State the blood parasite species.
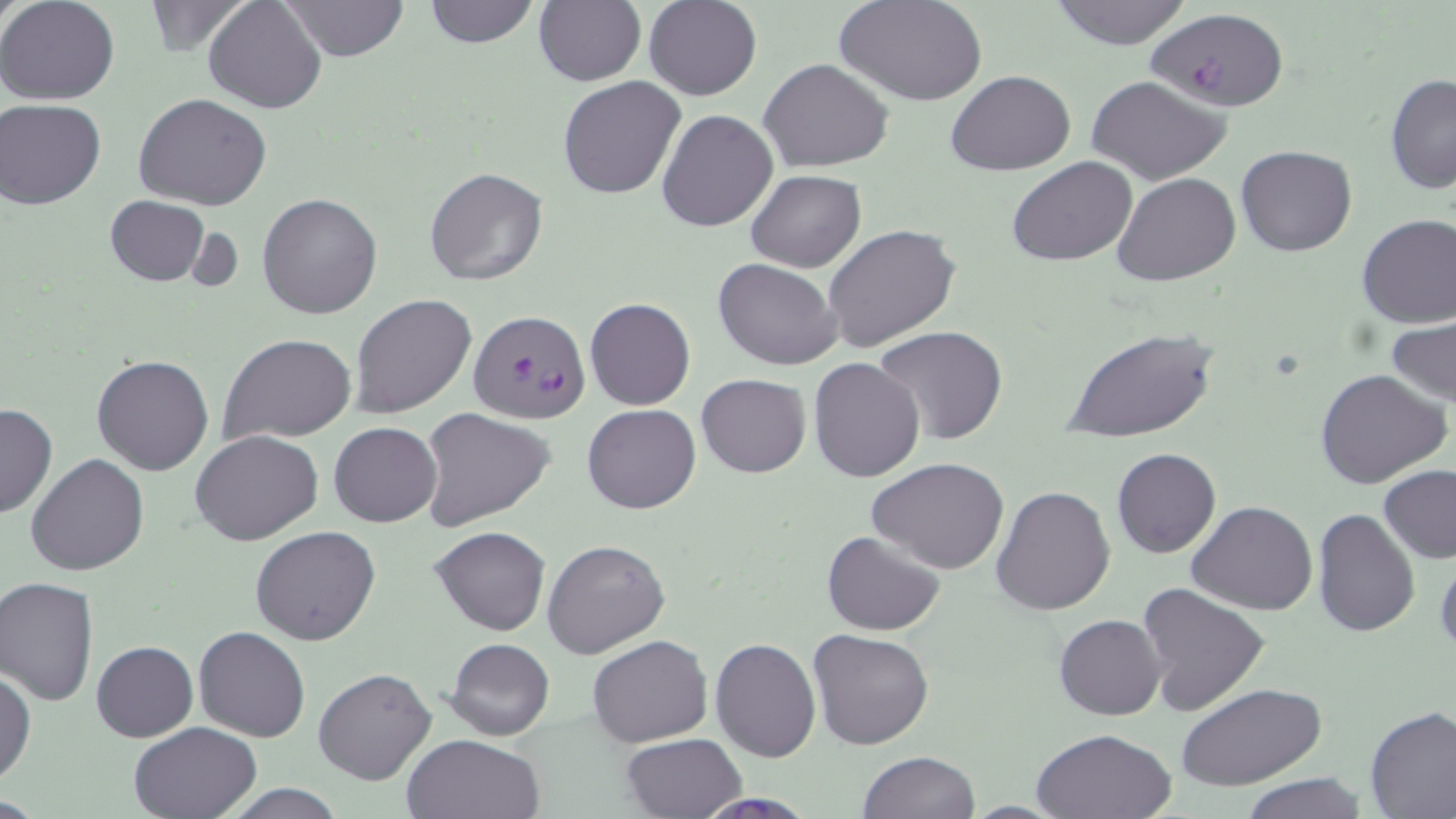
Plasmodium falciparum.

Approximate bounding boxes as (x1, y1, x2, y2) in pixels. Plasmodium falciparum-infected red blood cell locations: (468, 311, 590, 426). Uninfected red blood cell locations: (0, 0, 121, 105), (204, 0, 326, 115), (283, 0, 409, 61), (421, 0, 540, 49), (534, 0, 647, 88), (644, 0, 761, 100), (835, 0, 988, 107), (1045, 0, 1195, 49), (141, 1, 252, 54), (1147, 6, 1292, 113), (759, 58, 893, 170), (947, 71, 1076, 176), (1385, 71, 1456, 195), (557, 75, 685, 200), (1086, 76, 1232, 185), (134, 94, 273, 210), (1, 99, 105, 208), (658, 109, 779, 231), (1236, 145, 1357, 257), (1008, 156, 1138, 267), (423, 167, 549, 287), (745, 170, 866, 273), (1113, 173, 1241, 287), (257, 192, 383, 319), (105, 195, 211, 287), (1356, 213, 1456, 327), (824, 224, 961, 355), (714, 258, 841, 369), (350, 295, 477, 419), (584, 297, 695, 411), (1386, 315, 1456, 406), (872, 325, 1009, 446), (1065, 326, 1217, 445), (219, 333, 357, 445), (93, 356, 214, 475), (808, 356, 926, 482), (1314, 368, 1450, 489), (696, 373, 811, 477), (0, 403, 57, 519), (583, 404, 701, 514), (419, 409, 553, 533), (330, 422, 441, 528), (191, 429, 324, 545), (1111, 447, 1220, 558), (25, 453, 150, 575), (866, 457, 1010, 572), (1378, 465, 1456, 564), (990, 485, 1115, 616), (1186, 500, 1318, 617), (1311, 508, 1421, 639), (250, 525, 381, 645), (431, 525, 551, 635), (822, 530, 946, 636), (542, 537, 671, 660), (1434, 548, 1456, 660), (1, 576, 99, 703), (1137, 583, 1270, 716), (1054, 614, 1168, 719), (192, 626, 311, 742), (807, 629, 934, 750), (587, 635, 712, 747), (710, 637, 821, 762), (445, 638, 554, 740), (92, 640, 198, 741), (314, 667, 436, 785), (0, 668, 36, 786), (1176, 684, 1326, 791), (1364, 705, 1456, 817), (129, 721, 261, 818), (1030, 728, 1176, 818), (402, 733, 546, 819), (620, 734, 747, 819), (858, 750, 981, 819), (1241, 775, 1365, 819), (216, 783, 351, 818), (692, 792, 819, 818). Captured at 1000x magnification. Image is 1456×819 pixels. Single field of view. May-Grünwald-Giemsa stain. Thin blood smear. Optical microscopy.